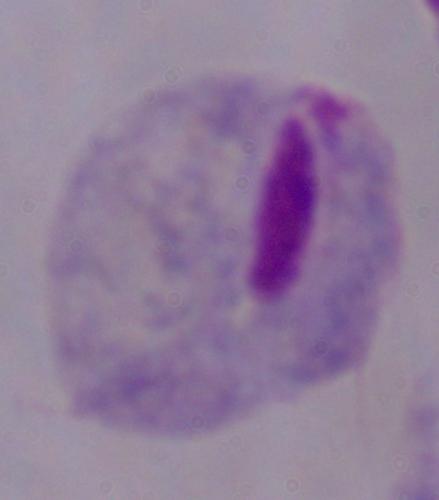

Summary:
  - Magnification: 1000x
  - Identification: trichomonad
  - Modality: micrograph